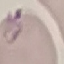
malaria_status: parasitized
stain: Giemsa
capture: smartphone through the microscope eyepiece
image_type: cell patch, automatically extracted from a larger field of view and resized to 64 × 64 pixels
preparation: thin blood film